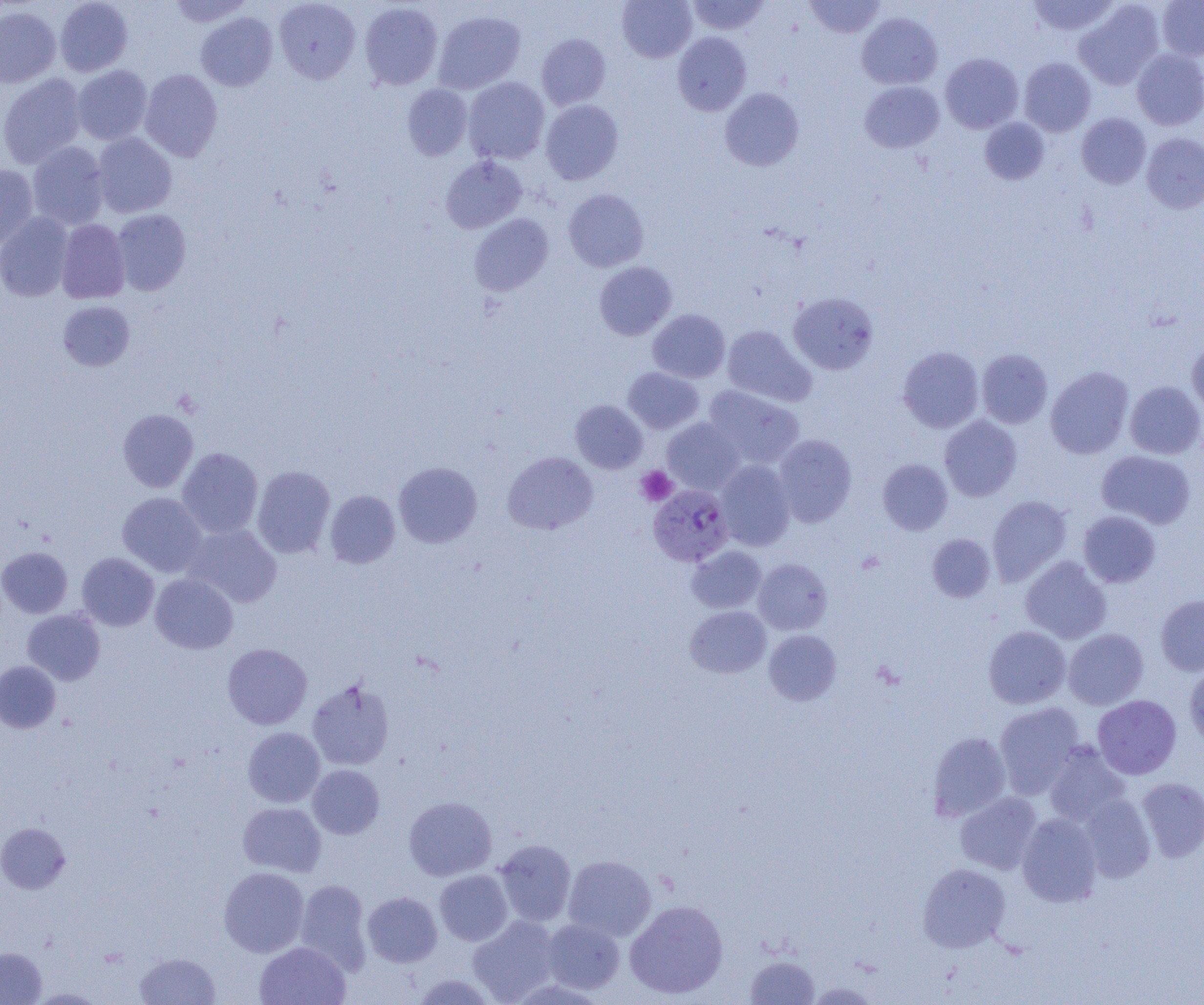

{
  "slide_level_diagnosis": "Plasmodium falciparum",
  "modality": "light microscopy",
  "preparation": "thin blood film",
  "image_size": "1204×1005 pixels",
  "magnification": "1000x",
  "platelet_locations": "approximate bounding boxes as (x1,y1)-(x2,y2) corner pairs in pixels: (636,466)-(677,506)",
  "plasmodium_falciparum_infected_red_blood_cell_locations": "approximate bounding boxes as (x1,y1)-(x2,y2) corner pairs in pixels: (648,485)-(733,566)",
  "uninfected_red_blood_cell_locations": "approximate bounding boxes as (x1,y1)-(x2,y2) corner pairs in pixels: (54,0)-(133,77), (168,0)-(252,27), (617,0)-(696,62), (687,0)-(770,35), (804,0)-(887,38), (1027,0)-(1120,37), (1157,0)-(1204,60), (274,1)-(360,84), (1074,1)-(1164,90), (360,2)-(442,90), (0,6)-(61,88), (433,10)-(525,94), (196,12)-(277,91), (857,12)-(942,89), (672,32)-(751,115), (536,34)-(611,110), (1132,49)-(1204,130), (940,53)-(1023,133), (1019,58)-(1096,136), (73,65)-(152,145), (140,69)-(223,161), (0,73)-(86,168), (463,77)-(549,164), (859,81)-(944,153), (402,84)-(472,161), (720,88)-(804,171), (541,100)-(623,184), (1076,113)-(1151,188), (980,118)-(1049,185), (92,133)-(177,217), (1141,133)-(1204,213), (28,141)-(109,230), (440,156)-(527,233), (0,164)-(39,250), (563,189)-(649,272), (111,209)-(191,295), (0,212)-(74,302), (469,214)-(554,296), (56,219)-(130,304), (594,261)-(677,340), (788,292)-(878,374), (58,301)-(134,371), (648,309)-(730,383), (722,325)-(816,407), (1187,341)-(1204,415), (898,347)-(984,433), (977,349)-(1052,428), (1045,366)-(1134,459), (623,367)-(704,434), (1125,381)-(1204,459), (704,385)-(805,469), (570,400)-(647,473), (117,408)-(198,493), (939,415)-(1022,501), (662,418)-(745,494), (774,434)-(857,527), (177,447)-(263,539), (1097,450)-(1196,528), (503,452)-(598,534), (878,459)-(953,534), (714,460)-(795,551), (393,462)-(482,548), (252,465)-(335,558), (325,490)-(400,569), (117,492)-(207,577), (987,495)-(1072,585), (1078,511)-(1161,587), (183,524)-(282,607), (927,533)-(995,602), (687,545)-(766,613), (0,546)-(72,617), (77,552)-(159,630), (1020,556)-(1111,644), (753,558)-(833,635), (150,573)-(238,654), (1156,595)-(1204,676), (685,605)-(771,678), (22,609)-(106,685), (983,626)-(1071,709), (1063,628)-(1148,709), (764,629)-(841,705), (222,643)-(312,729), (0,661)-(60,733), (1184,664)-(1204,749), (307,679)-(394,770), (1092,694)-(1181,779), (994,702)-(1085,799), (243,727)-(325,807), (927,732)-(1011,821), (1043,741)-(1131,826), (307,765)-(384,839), (1136,776)-(1204,862), (955,792)-(1042,875), (1078,794)-(1155,883), (404,796)-(497,880), (238,802)-(326,876), (1017,813)-(1102,906), (0,823)-(70,894), (494,839)-(576,926), (563,855)-(656,941), (917,863)-(1011,952), (219,867)-(309,956), (434,869)-(512,945), (295,879)-(372,973), (362,891)-(442,966), (624,900)-(728,999), (468,915)-(562,1004), (541,919)-(625,994), (254,942)-(351,1005), (0,947)-(46,1004), (135,953)-(220,1005), (744,954)-(819,1004), (411,973)-(499,1005)",
  "field_of_view": "single"
}